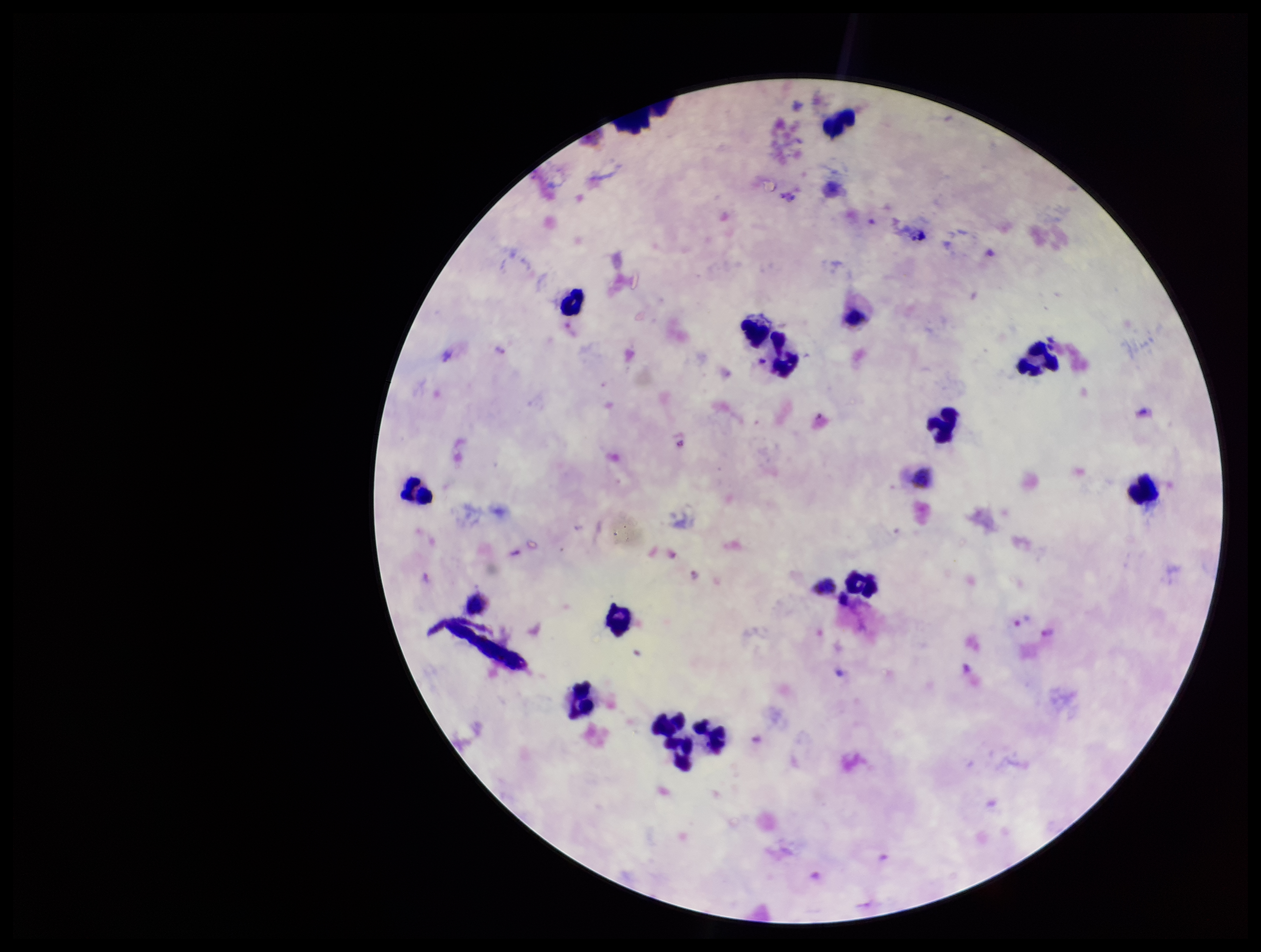

Leukocyte count: 13. Photographed through the microscope eyepiece with a smartphone camera. Image is 1261×952 pixels. Patient malaria status: positive. Preparation: thick smear. Parasite count: 2. Single field of view. Species reported for this patient: Plasmodium vivax. Giemsa stain. Plasmodium parasites: seen.